Comment on the morphology of the red blood cells.
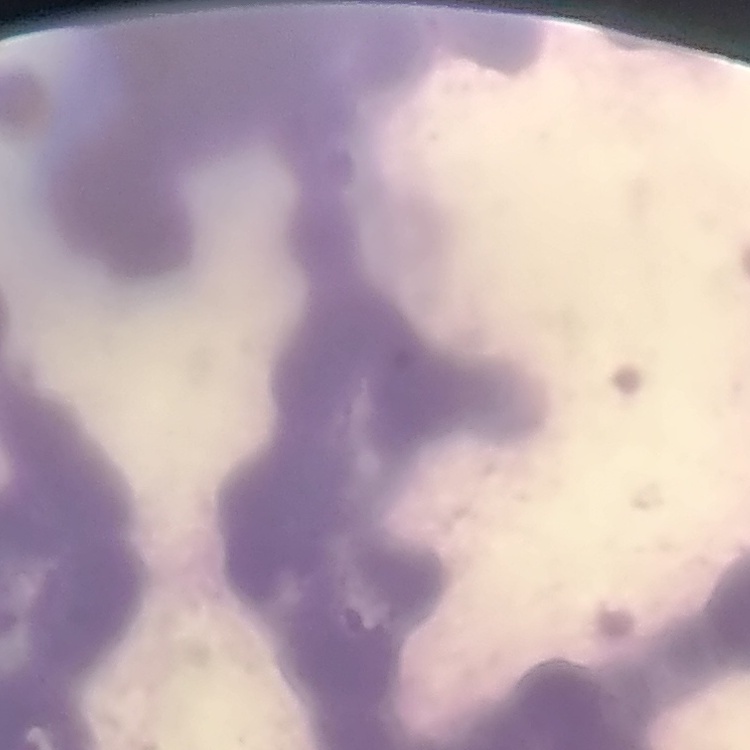

They show rouleaux formation.

Thin blood smear. Square crop of a larger photomicrograph. Field's or Giemsa stain.